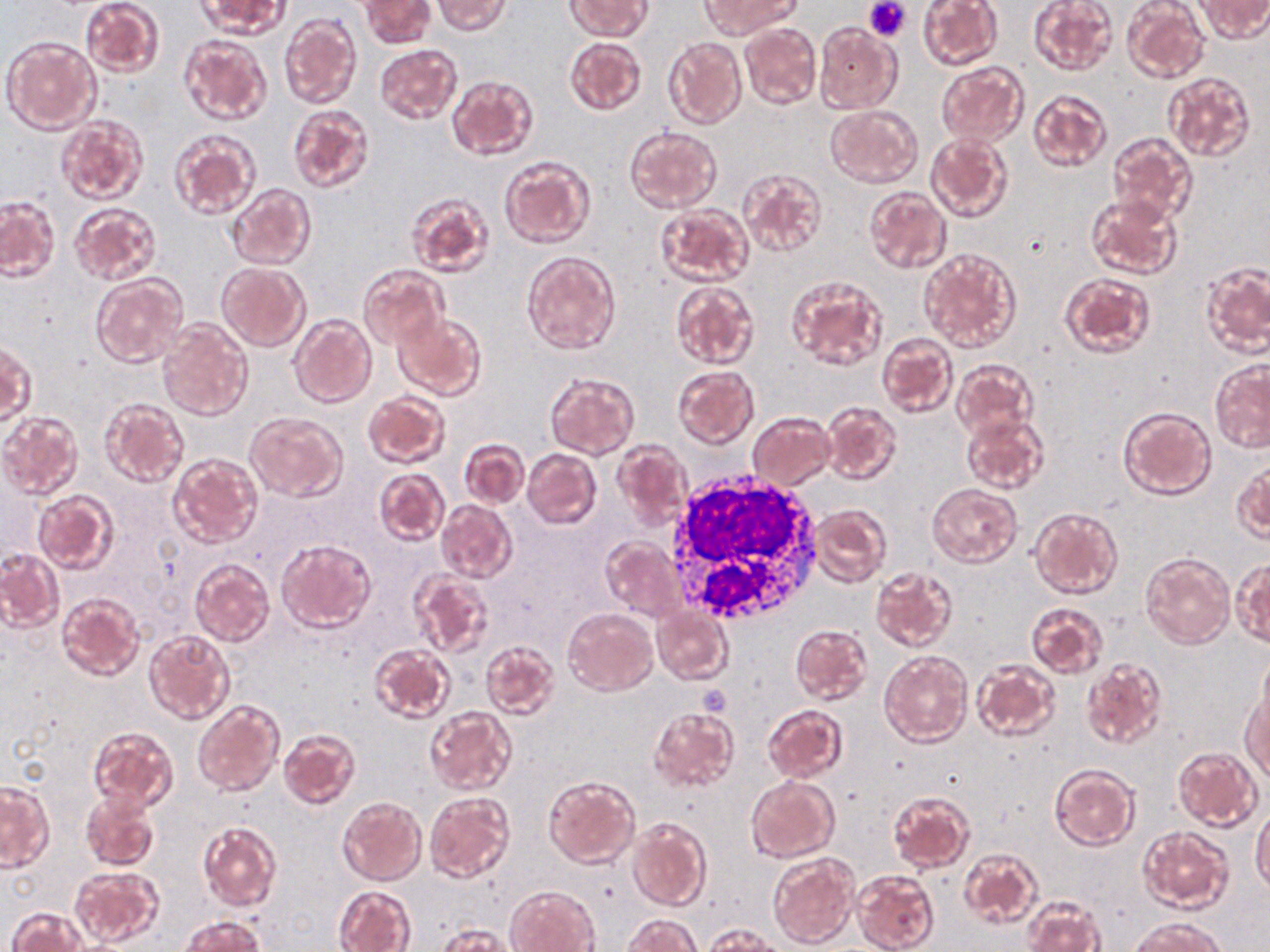
slide-level diagnosis = negative for blood parasites
stain = May-Grünwald-Giemsa
image size = 1270×952 pixels
uninfected red blood cell locations = approximate bounding boxes as (x1,y1)-(x2,y2) corner pairs in pixels: (80,0)-(165,78), (197,0)-(290,38), (360,0)-(434,49), (566,0)-(651,40), (917,0)-(1002,70), (1028,0)-(1117,75), (1121,0)-(1209,84), (1197,0)-(1269,41), (433,1)-(512,34), (700,2)-(795,37), (280,12)-(361,109), (814,22)-(900,113), (740,24)-(821,109), (179,34)-(271,125), (3,36)-(101,134), (565,36)-(646,116), (663,37)-(746,128), (375,44)-(462,123), (935,61)-(1027,147), (1164,70)-(1256,162), (446,75)-(539,160), (1027,89)-(1112,173), (287,103)-(376,194), (825,105)-(923,187), (56,116)-(148,205), (625,125)-(722,213), (168,128)-(261,220), (1108,130)-(1198,224), (925,132)-(1013,223), (499,155)-(595,249), (738,167)-(827,258), (227,184)-(316,270), (863,186)-(952,274), (406,190)-(494,277), (1077,192)-(1173,357), (1086,194)-(1184,279), (1,197)-(59,281), (69,202)-(162,286), (655,204)-(753,286), (919,248)-(1021,352), (523,251)-(621,354), (218,263)-(310,350), (1201,263)-(1269,355), (357,265)-(447,349), (1057,271)-(1157,359), (91,273)-(188,367), (786,275)-(888,372), (669,282)-(760,370), (393,310)-(488,401), (288,314)-(375,408), (157,319)-(253,421), (877,332)-(955,417), (0,343)-(35,428), (952,359)-(1037,441), (1209,359)-(1270,452), (673,366)-(760,449), (544,372)-(640,458), (362,390)-(450,469), (99,398)-(189,488), (822,402)-(901,485), (1118,406)-(1216,500), (1,411)-(84,500), (244,411)-(347,502), (747,411)-(835,490), (961,412)-(1049,496), (459,439)-(529,507), (613,440)-(692,530), (522,448)-(602,530), (167,453)-(263,548), (1232,461)-(1269,543), (374,469)-(449,546), (928,484)-(1021,568), (33,491)-(119,574), (436,500)-(517,583), (810,504)-(891,586), (1028,505)-(1123,600), (600,536)-(684,621), (275,538)-(376,632), (0,549)-(64,631), (1140,552)-(1234,648), (189,557)-(274,647), (1233,558)-(1270,648), (870,566)-(956,652), (408,571)-(495,660), (57,594)-(145,682), (1026,601)-(1109,678), (652,606)-(732,683), (563,608)-(657,695), (790,624)-(872,705), (143,629)-(235,725), (480,639)-(560,718), (368,644)-(455,724), (880,651)-(971,748), (1257,652)-(1270,736), (1082,658)-(1167,749), (970,659)-(1060,742), (1241,684)-(1269,781), (193,700)-(284,795), (762,704)-(848,782), (424,707)-(516,795), (649,707)-(739,793), (87,726)-(178,811), (279,728)-(362,810), (1172,746)-(1263,832), (1049,763)-(1139,850), (543,775)-(640,869), (745,776)-(839,863), (1,783)-(53,872), (887,789)-(974,873), (80,790)-(160,872), (425,791)-(515,883), (337,796)-(426,885), (1251,807)-(1270,892), (627,818)-(711,912), (197,822)-(281,912), (1136,826)-(1234,914), (958,848)-(1042,929), (768,851)-(860,950), (70,866)-(165,949), (853,868)-(940,952), (506,884)-(599,952), (333,885)-(417,952), (1023,895)-(1106,952), (6,907)-(90,952), (623,914)-(702,951), (180,916)-(264,951), (1130,917)-(1228,952), (436,923)-(518,951), (701,923)-(782,951)
preparation = thin blood smear
white blood cell locations = approximate bounding boxes as (x1,y1)-(x2,y2) corner pairs in pixels: (663,471)-(822,624)
modality = optical microscopy
field of view = single
platelet locations = approximate bounding boxes as (x1,y1)-(x2,y2) corner pairs in pixels: (865,0)-(909,40)
magnification = 1000x